Assess this cell for malaria.
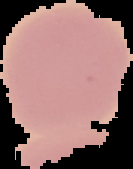

Uninfected.

Summary:
  - Image size: 133×169 pixels
  - Preparation: thin blood smear
  - Image type: segmented cell region with the area outside set to black